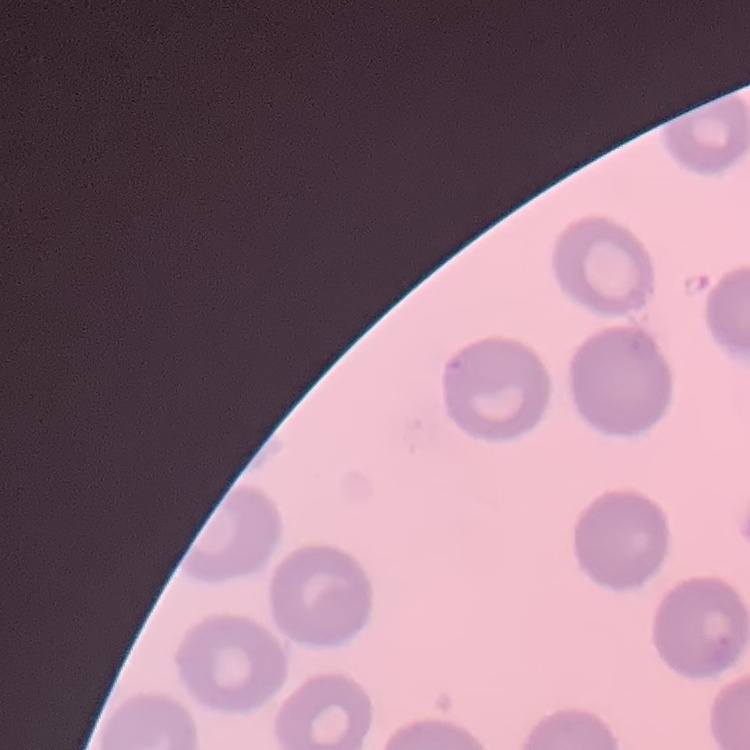
The erythrocytes exhibit no rouleaux formation. Thin peripheral smear. Field's or Giemsa stain. Square crop of a larger photomicrograph.